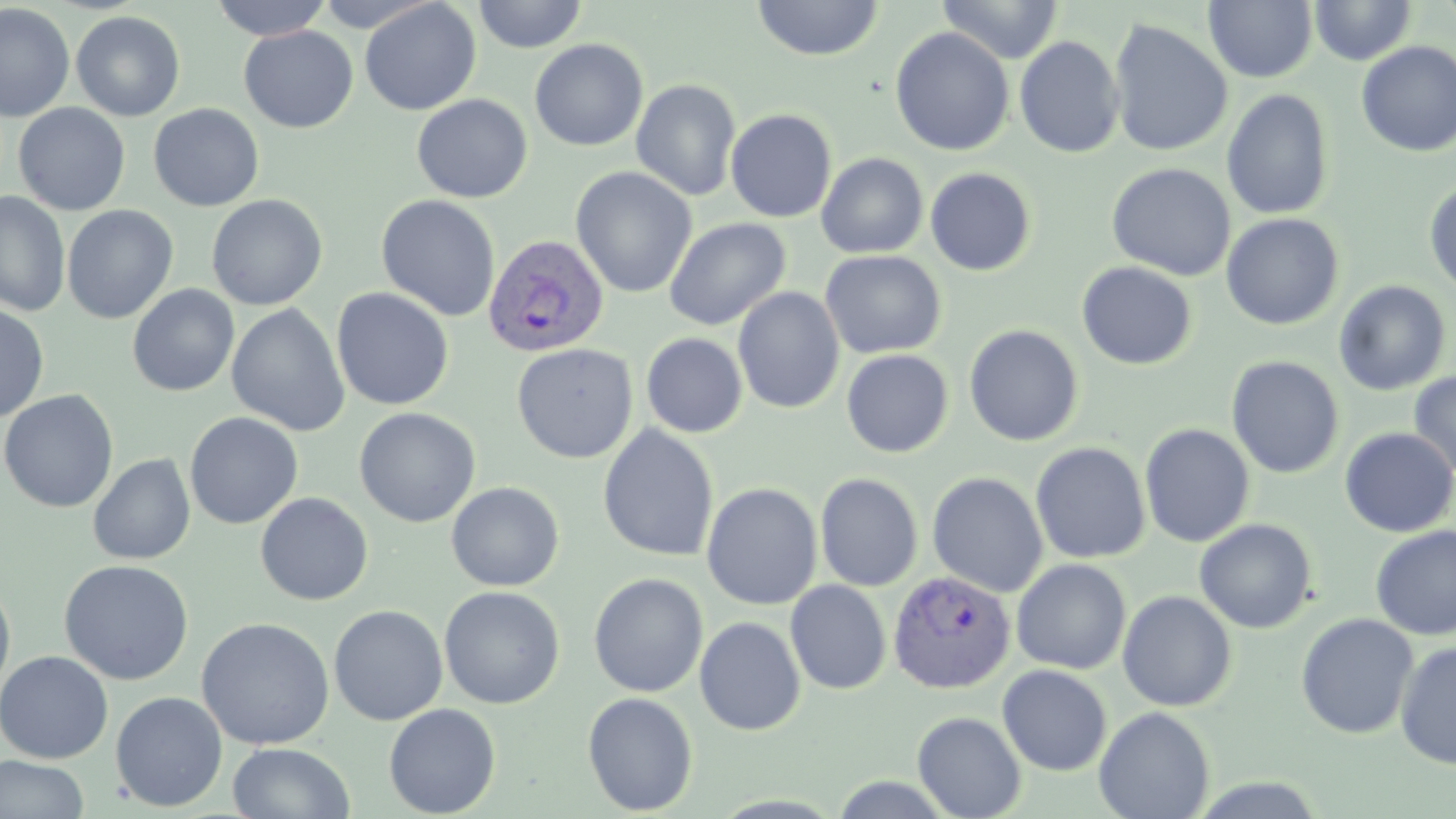 Approximate bounding boxes as [x1, y1, x2, y2] in pixels. Plasmodium vivax-infected red blood cell locations: [483, 234, 610, 358], [888, 570, 1017, 695]. Uninfected red blood cell locations: [209, 0, 333, 40], [473, 0, 589, 53], [938, 0, 1063, 64], [1309, 0, 1417, 65], [359, 1, 481, 116], [752, 1, 884, 61], [1204, 1, 1318, 83], [0, 3, 74, 122], [71, 10, 186, 121], [1107, 18, 1233, 157], [238, 25, 359, 133], [889, 27, 1015, 157], [1013, 35, 1126, 159], [529, 39, 648, 152], [1356, 42, 1456, 158], [630, 79, 742, 201], [1221, 88, 1334, 220], [411, 93, 532, 203], [13, 103, 131, 216], [148, 103, 265, 212], [725, 108, 837, 223], [816, 152, 928, 258], [817, 160, 1045, 264], [1106, 162, 1236, 281], [570, 167, 697, 298], [925, 167, 1036, 276], [1424, 181, 1456, 297], [0, 191, 71, 317], [206, 194, 328, 310], [376, 194, 500, 322], [62, 205, 178, 324], [1221, 213, 1343, 331], [664, 217, 791, 332], [820, 250, 946, 359], [1076, 261, 1197, 370], [1333, 279, 1451, 396], [127, 284, 240, 397], [732, 286, 845, 414], [331, 288, 454, 410], [0, 302, 50, 422], [226, 303, 350, 437], [963, 324, 1084, 446], [641, 333, 748, 438], [512, 342, 638, 464], [841, 349, 953, 458], [1226, 355, 1345, 479], [1407, 371, 1456, 481], [0, 389, 119, 514], [354, 407, 480, 527], [184, 411, 303, 529], [1139, 423, 1255, 547], [597, 424, 719, 563], [1339, 427, 1456, 537], [1030, 441, 1151, 563], [87, 453, 196, 565], [927, 471, 1049, 597], [815, 472, 924, 591], [446, 481, 565, 592], [701, 482, 823, 610], [255, 492, 373, 606], [1194, 518, 1317, 634], [1370, 525, 1456, 642], [1011, 558, 1131, 674], [58, 559, 195, 686], [589, 573, 708, 697], [0, 576, 16, 701], [785, 580, 891, 695], [439, 586, 565, 709], [1117, 590, 1238, 712], [328, 605, 448, 726], [1295, 612, 1419, 739], [196, 617, 335, 750], [694, 617, 806, 735], [1395, 640, 1456, 769], [0, 650, 114, 764], [997, 664, 1112, 776], [110, 691, 228, 812], [582, 692, 698, 815], [383, 703, 501, 817], [1093, 706, 1215, 819], [912, 711, 1027, 819], [227, 742, 356, 818], [0, 756, 90, 817]. Slide-level diagnosis: Plasmodium vivax. Single field of view. 1000x magnification. May-Grünwald-Giemsa stain. Thin blood film. Optical microscopy. Image is 1456×819 pixels.